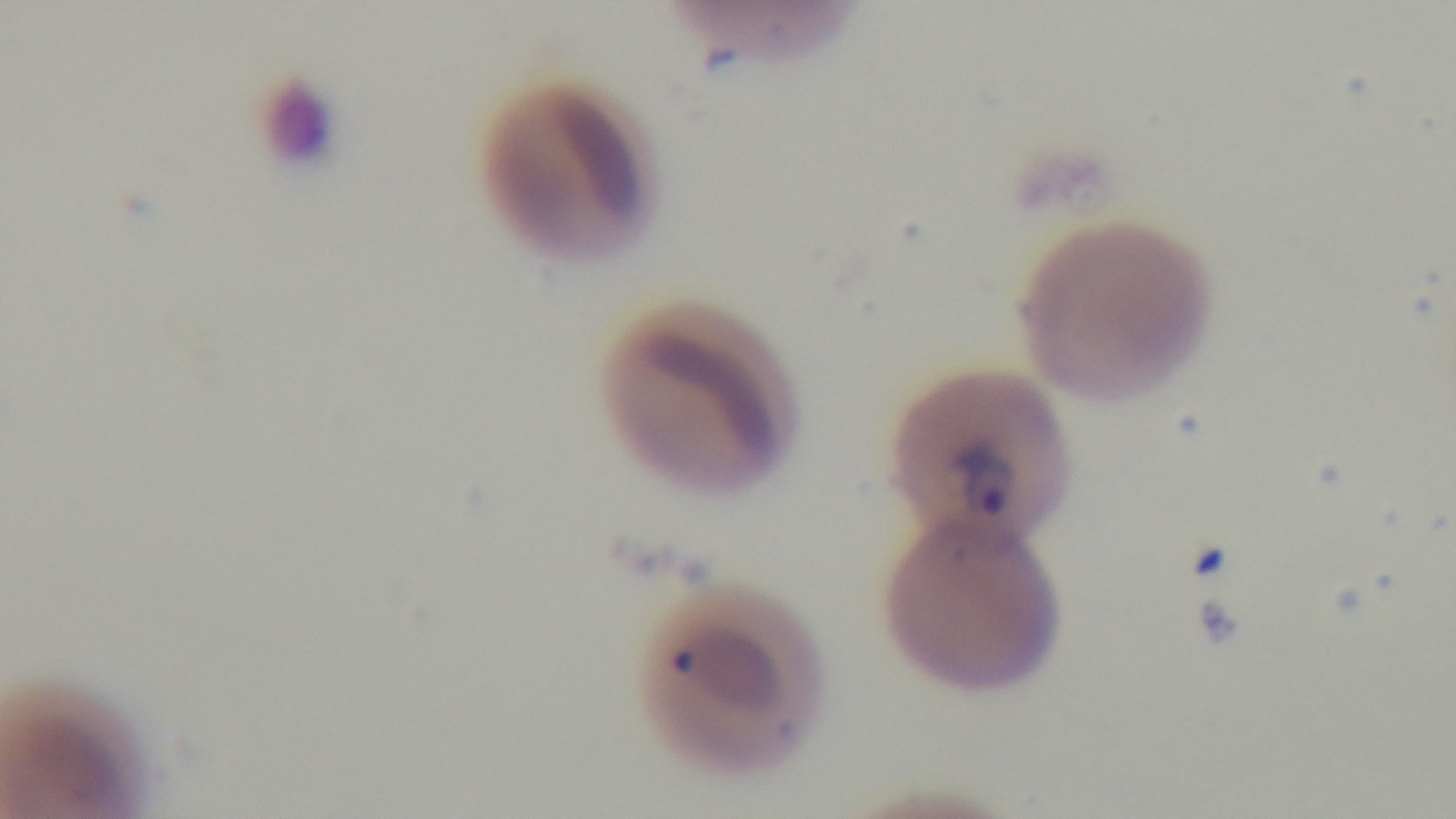

Summary:
  - Preparation: thin blood film
  - Capture: mounted 4K digital camera
  - Malaria status: positive
  - Field of view: one from the slide
  - Objective: 100x oil immersion
  - Stain: Giemsa
  - Modality: light microscopy